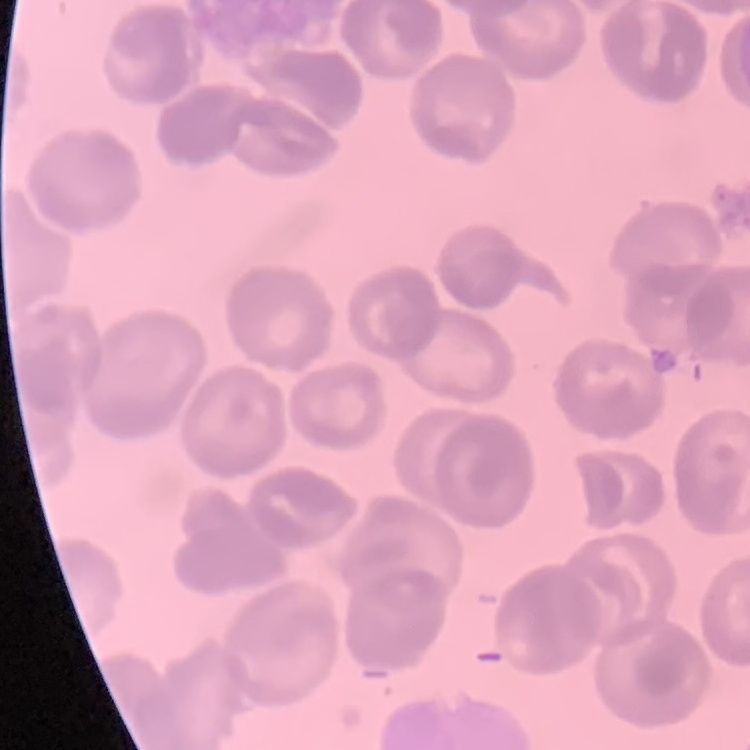

red blood cell morphology = no rouleaux formation
image type = one tile cut from a larger photomicrograph
stain = Field's or Giemsa
preparation = thin blood film